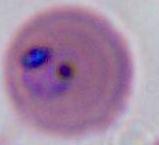

Photomicrograph. A Plasmodium parasite is shown. Captured at either 400x or 1000x magnification.